Name the parasite shown.
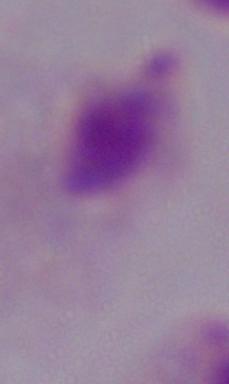
A trichomonad.

modality = photomicrograph
magnification = 1000x